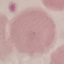 Result: negative for malaria parasites. Photographed with a smartphone camera at the microscope eyepiece. Thin smear of blood. Automatically extracted cell patch, resized to 64 × 64 pixels. Giemsa stain.